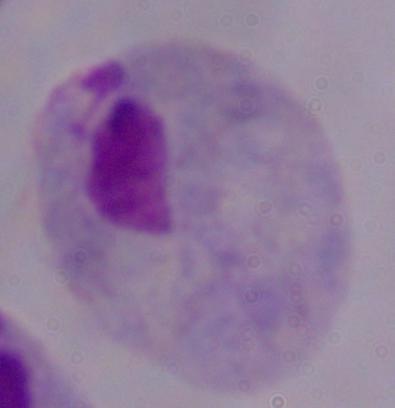
Summary:
  - Modality: photomicrograph
  - Identification: trichomonad
  - Magnification: 1000x